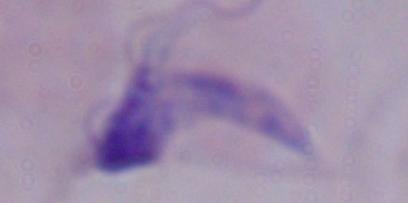
{
  "modality": "micrograph",
  "magnification": "1000x",
  "identification": "trypanosome"
}